Outline each uninfected red blood cell.
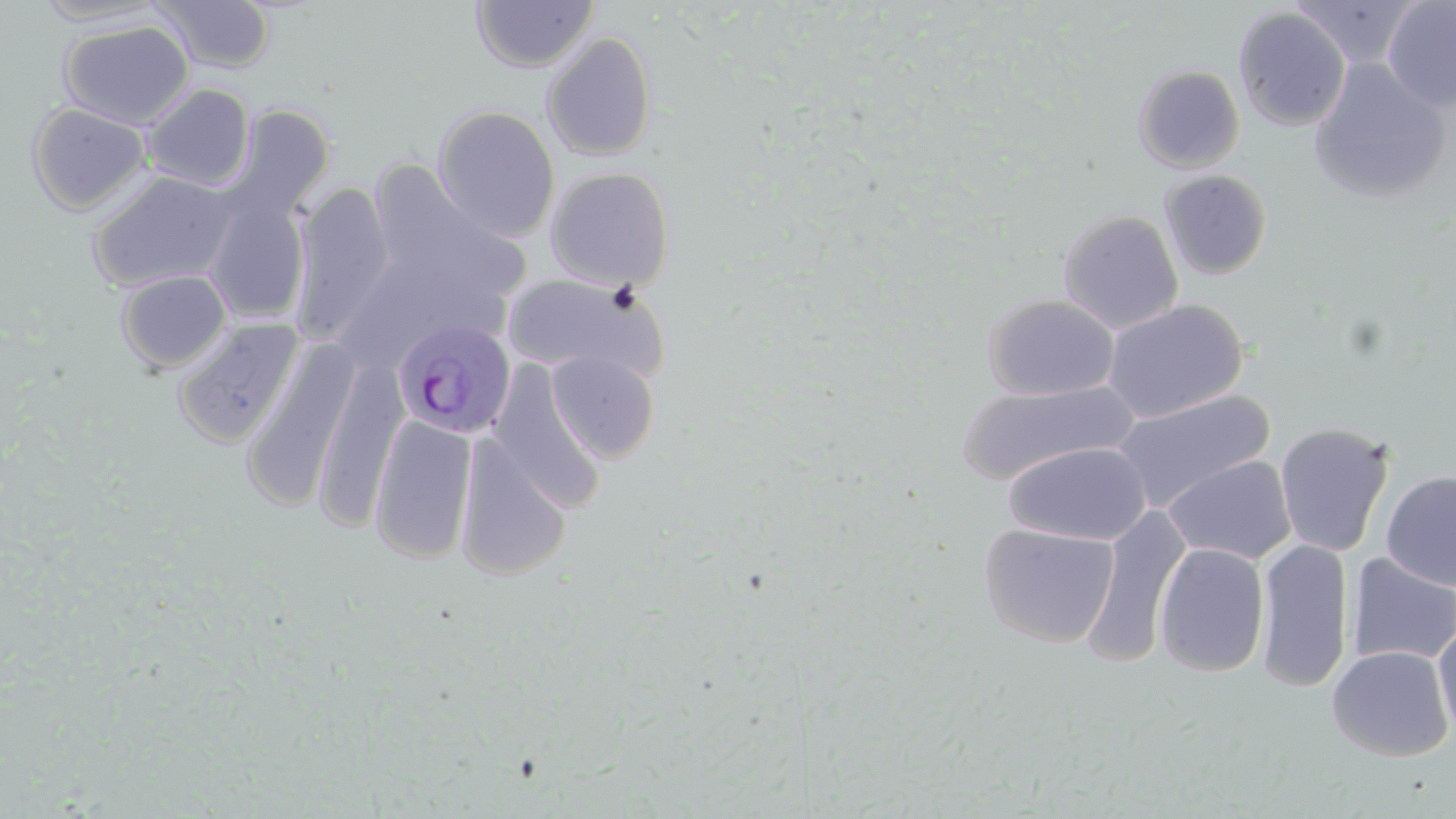
Approximate bounding boxes as (x1, y1, x2, y2) in pixels.
Uninfected red blood cells: (33, 0, 168, 26), (1291, 0, 1421, 69), (1381, 0, 1456, 112), (154, 1, 276, 73), (471, 1, 598, 73), (1233, 7, 1351, 131), (58, 20, 194, 130), (541, 31, 657, 161), (1308, 59, 1450, 204), (1132, 64, 1245, 172), (142, 83, 255, 191), (27, 103, 151, 215), (230, 104, 335, 218), (433, 105, 559, 241), (362, 159, 530, 318), (545, 166, 675, 291), (87, 170, 239, 293), (1159, 170, 1273, 280), (291, 182, 393, 345), (204, 195, 311, 324), (1058, 209, 1184, 334), (116, 270, 231, 373), (502, 271, 664, 380), (983, 293, 1120, 401), (1103, 299, 1247, 422), (173, 317, 303, 448), (241, 339, 360, 514), (546, 350, 660, 463), (311, 357, 408, 534), (489, 361, 606, 513), (955, 379, 1136, 485), (1111, 390, 1275, 513), (368, 413, 478, 566), (1274, 421, 1395, 558), (455, 434, 572, 581), (1005, 442, 1151, 546), (1163, 455, 1297, 565), (1380, 469, 1456, 590), (1082, 506, 1191, 667), (979, 522, 1120, 648), (1255, 537, 1353, 692), (1154, 542, 1270, 677), (1346, 552, 1456, 667), (1433, 624, 1456, 740), (1326, 645, 1454, 762).

Summary:
  - Plasmodium ovale-infected red blood cell locations: (392, 321, 516, 442)
  - Slide-level diagnosis: Plasmodium ovale
  - Image size: 1456×819 pixels
  - Field of view: one of a larger specimen
  - Preparation: thin blood film
  - Stain: May-Grünwald-Giemsa
  - Modality: light microscopy
  - Magnification: 1000x